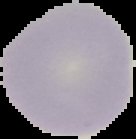
image type = segmented cell region with the area outside set to black
malaria status = uninfected
image size = 136×139 pixels
preparation = thin blood smear